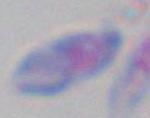

Summary:
  - Identification: Toxoplasma gondii
  - Magnification: 1000x
  - Modality: photomicrograph